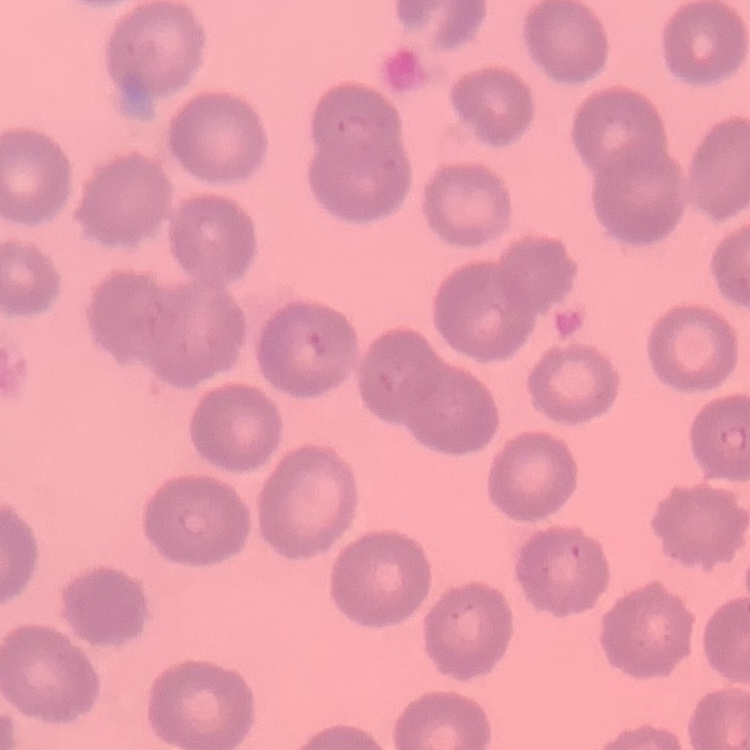 The red blood cells exhibit no rouleaux formation. Thin blood film. Square crop of a larger photomicrograph. Stained with either Field's or Giemsa.